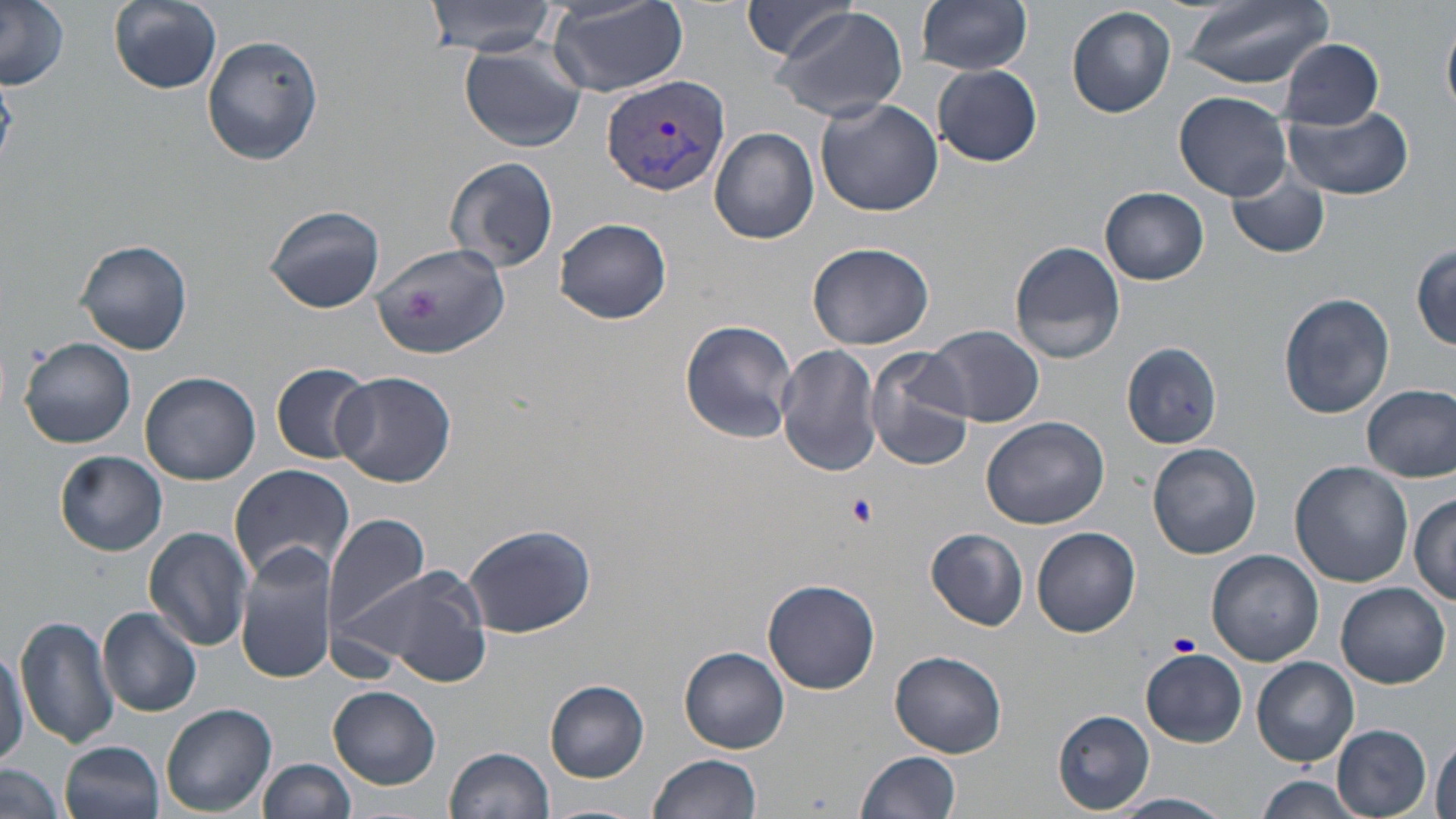

Approximate bounding boxes as (x1,y1)-(x2,y2) corner pairs in pixels. Plasmodium vivax-infected red blood cell locations: (602,76)-(732,198). Uninfected red blood cell locations: (0,0)-(69,88), (109,0)-(223,93), (426,0)-(562,54), (916,0)-(1033,74), (1177,0)-(1336,87), (740,1)-(863,60), (546,2)-(689,97), (770,5)-(909,123), (1067,5)-(1177,118), (1443,20)-(1456,118), (200,35)-(324,165), (1279,39)-(1388,128), (458,41)-(586,153), (932,64)-(1043,166), (1174,92)-(1291,200), (816,99)-(945,218), (1282,104)-(1414,200), (709,127)-(819,245), (443,156)-(560,273), (1224,167)-(1333,260), (1101,187)-(1209,284), (265,205)-(387,314), (556,217)-(672,324), (76,239)-(192,356), (1008,240)-(1125,364), (808,241)-(934,349), (373,242)-(510,359), (1412,243)-(1455,348), (1279,292)-(1395,419), (679,318)-(800,443), (924,328)-(1044,427), (19,337)-(136,449), (1120,342)-(1223,450), (776,343)-(882,477), (864,347)-(976,470), (271,362)-(374,463), (141,371)-(260,485), (328,371)-(458,488), (1363,384)-(1456,481), (981,415)-(1109,529), (1147,443)-(1262,559), (56,451)-(167,556), (1290,462)-(1413,587), (227,464)-(357,586), (1410,492)-(1456,605), (323,514)-(431,636), (464,523)-(595,635), (143,527)-(253,651), (1031,527)-(1140,638), (926,528)-(1027,631), (235,543)-(339,685), (1208,549)-(1323,666), (340,560)-(491,685), (762,578)-(883,694), (1335,583)-(1450,687), (98,608)-(203,716), (16,613)-(121,751), (0,638)-(28,772), (680,647)-(789,753), (1140,649)-(1246,749), (889,650)-(1008,759), (1252,657)-(1359,766), (544,679)-(651,783), (329,685)-(441,790), (161,703)-(276,816), (1054,709)-(1155,814), (1332,723)-(1432,817), (1429,739)-(1455,819), (61,741)-(165,819), (446,746)-(555,819), (856,751)-(962,819), (647,755)-(761,819), (260,759)-(357,818), (1,762)-(65,819), (1255,777)-(1363,817), (1113,793)-(1233,817), (540,801)-(645,819). Platelet locations: (404,287)-(443,320), (845,494)-(876,526), (1169,631)-(1202,657). Slide-level diagnosis: Plasmodium vivax. Image is 1456×819 pixels. Captured at 1000x magnification. One field of a larger specimen. Optical microscopy. May-Grünwald-Giemsa stain. Thin blood film.